Give the extent of all Plasmodium vivax-infected red blood cells.
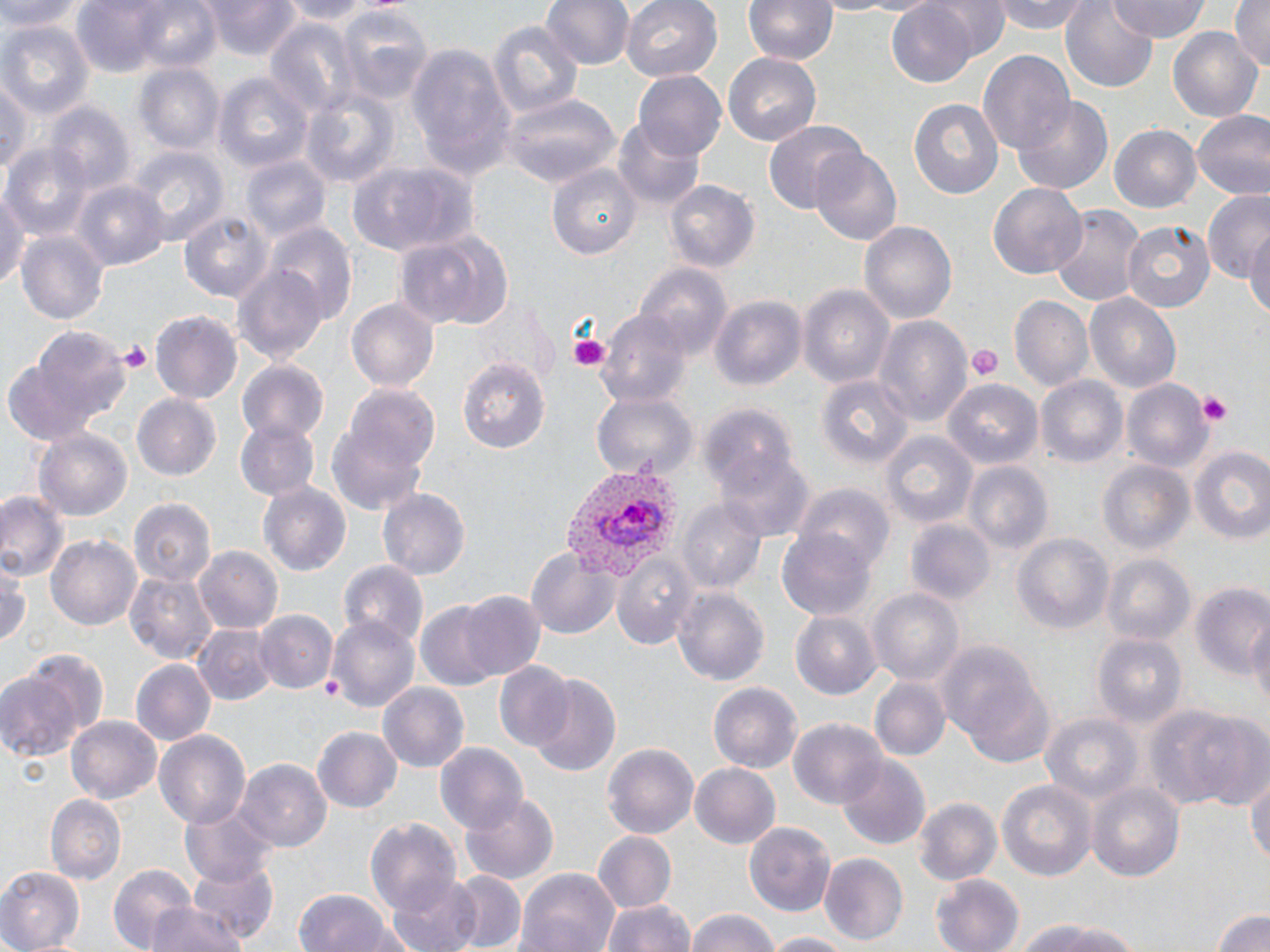
Approximate bounding boxes as (x1, y1, x2, y2) in pixels.
Plasmodium vivax-infected red blood cells: (559, 463, 679, 580).

{
  "slide_level_diagnosis": "Plasmodium vivax",
  "platelet_locations": "approximate bounding boxes as (x1, y1, x2, y2) in pixels: (568, 331, 613, 371), (116, 339, 152, 371), (968, 345, 1001, 384), (1194, 391, 1235, 425)",
  "uninfected_red_blood_cell_locations": "approximate bounding boxes as (x1, y1, x2, y2) in pixels: (2, 0, 78, 34), (69, 0, 213, 77), (276, 0, 377, 23), (544, 0, 633, 70), (623, 0, 722, 83), (743, 0, 837, 65), (929, 0, 1009, 59), (994, 0, 1092, 34), (1109, 0, 1211, 42), (1229, 0, 1269, 73), (201, 1, 303, 61), (884, 3, 978, 88), (1061, 3, 1159, 90), (338, 5, 435, 101), (486, 17, 583, 122), (264, 18, 358, 121), (0, 21, 93, 118), (1169, 27, 1263, 126), (407, 46, 514, 180), (977, 50, 1076, 160), (724, 53, 821, 144), (135, 63, 226, 155), (634, 71, 727, 162), (214, 72, 313, 174), (0, 78, 28, 183), (299, 88, 401, 189), (503, 93, 618, 188), (1014, 96, 1113, 193), (908, 97, 1004, 200), (44, 102, 133, 198), (1191, 110, 1270, 202), (613, 119, 705, 210), (765, 120, 866, 214), (1109, 125, 1202, 214), (6, 143, 93, 235), (810, 146, 903, 244), (132, 149, 227, 245), (241, 156, 331, 243), (347, 162, 478, 258), (548, 164, 641, 260), (72, 180, 167, 270), (662, 180, 757, 275), (0, 183, 28, 292), (988, 185, 1087, 278), (1198, 192, 1268, 279), (1048, 204, 1143, 305), (180, 210, 275, 302), (861, 220, 957, 325), (1121, 220, 1215, 314), (263, 221, 356, 322), (1246, 226, 1270, 326), (17, 228, 108, 324), (395, 228, 513, 331), (233, 263, 328, 367), (636, 264, 730, 356), (799, 287, 894, 389), (1086, 293, 1182, 394), (710, 296, 804, 392), (1009, 297, 1094, 392), (346, 298, 439, 392), (478, 298, 558, 384), (598, 310, 691, 409), (151, 311, 242, 403), (873, 315, 971, 426), (9, 329, 130, 438), (457, 358, 549, 455), (237, 361, 328, 444), (816, 376, 913, 477), (1037, 376, 1129, 470), (1121, 379, 1215, 475), (943, 381, 1043, 472), (326, 385, 439, 515), (591, 390, 695, 479), (132, 394, 221, 481), (699, 402, 797, 496), (234, 418, 319, 500), (36, 428, 132, 522), (882, 432, 977, 529), (717, 441, 811, 538), (1190, 444, 1270, 547), (1099, 460, 1195, 556), (962, 461, 1052, 555), (259, 484, 351, 577), (377, 487, 470, 578), (796, 488, 893, 577), (0, 491, 66, 581), (129, 498, 214, 585), (678, 501, 766, 593), (908, 520, 995, 605), (776, 530, 875, 622), (1010, 533, 1111, 633), (46, 535, 142, 632), (194, 545, 283, 634), (525, 545, 619, 638), (611, 551, 699, 650), (1102, 555, 1195, 646), (340, 563, 429, 654), (1, 564, 29, 650), (124, 571, 216, 664), (1189, 582, 1269, 676), (674, 585, 770, 684), (867, 587, 964, 687), (458, 592, 544, 681), (415, 603, 506, 690), (254, 610, 337, 694), (1245, 611, 1270, 715), (792, 613, 879, 698), (328, 615, 419, 713), (193, 624, 274, 706), (1093, 634, 1188, 730), (935, 637, 1051, 764), (132, 661, 215, 746), (494, 663, 572, 750), (0, 670, 83, 763), (528, 675, 621, 780), (870, 678, 952, 763), (708, 681, 801, 771), (377, 683, 469, 771), (1151, 703, 1269, 812), (1039, 714, 1142, 805), (67, 716, 163, 805), (790, 717, 888, 807), (312, 727, 402, 814), (153, 732, 252, 828), (601, 743, 699, 838), (436, 744, 528, 837), (836, 755, 932, 852), (237, 760, 330, 853), (690, 763, 782, 850), (1246, 764, 1270, 878), (996, 776, 1097, 881), (1086, 780, 1186, 884), (45, 793, 126, 883), (461, 793, 561, 885), (913, 796, 1002, 886), (182, 800, 278, 884), (365, 815, 463, 915), (743, 822, 836, 915), (593, 830, 677, 911), (819, 853, 909, 943), (185, 858, 278, 944), (106, 862, 201, 950), (517, 869, 619, 952), (0, 870, 83, 952), (448, 871, 525, 952), (390, 874, 484, 952), (930, 874, 1025, 952), (291, 888, 401, 952), (600, 898, 695, 952), (143, 902, 253, 952), (1211, 905, 1270, 952), (684, 908, 785, 952), (1008, 919, 1151, 952), (764, 932, 852, 952)",
  "preparation": "thin blood film",
  "modality": "light microscopy",
  "stain": "May-Grünwald-Giemsa",
  "magnification": "1000x",
  "image_size": "1270×952 pixels",
  "field_of_view": "single"
}